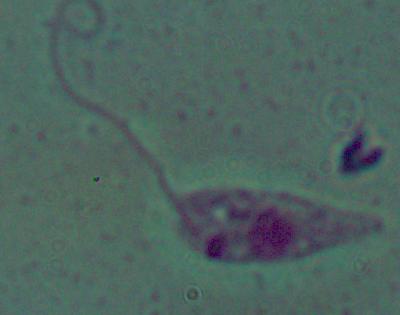
Captured at 1000x magnification. Photomicrograph. A Leishmania parasite is shown.